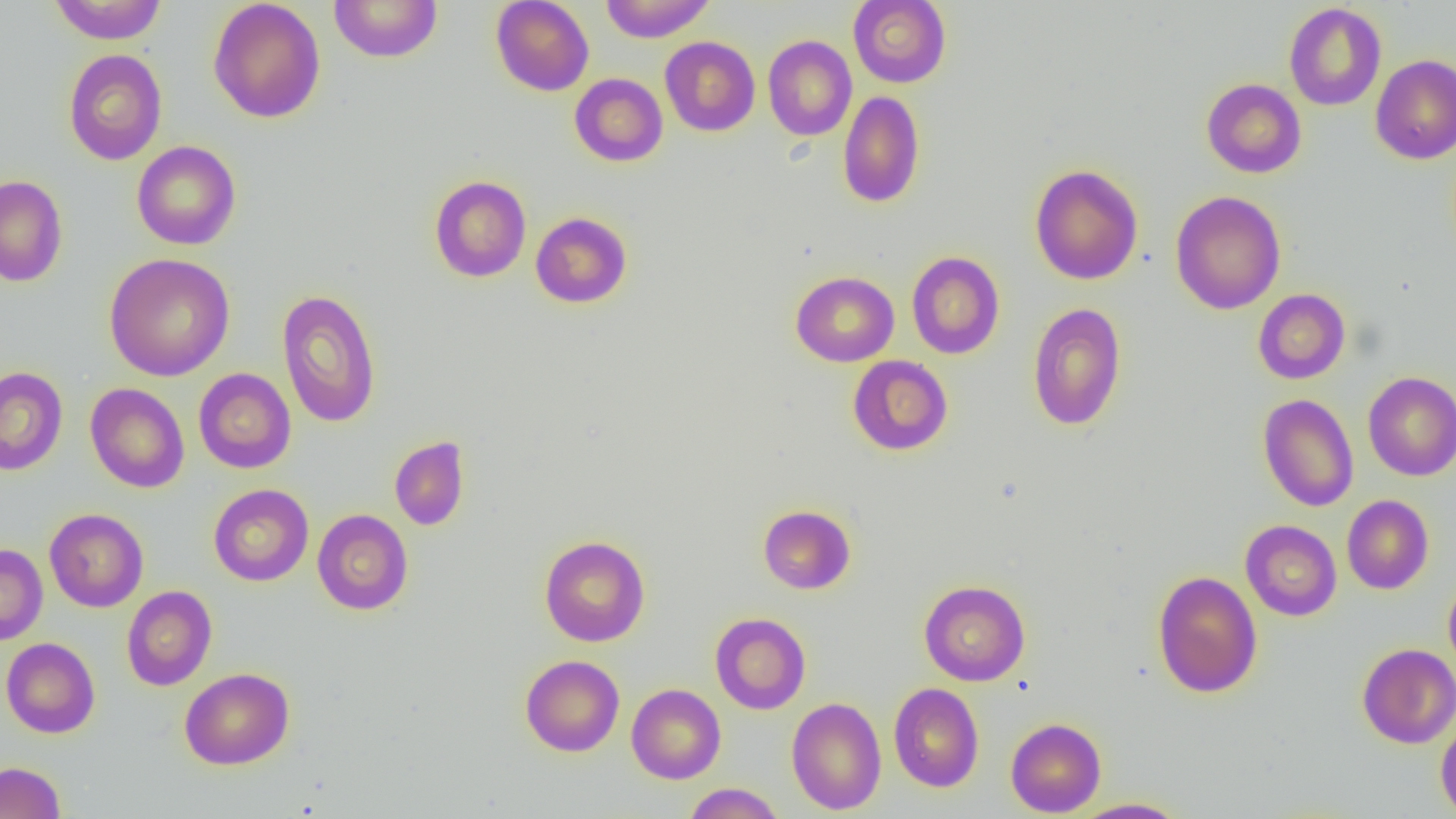

slide-level diagnosis = no evidence of blood parasites
uninfected red blood cell locations = approximate bounding boxes as (x1,y1)-(x2,y2) corner pairs in pixels: (48,0)-(168,44), (208,0)-(326,123), (490,0)-(594,96), (600,0)-(715,42), (848,0)-(951,88), (329,1)-(443,63), (1284,3)-(1386,110), (762,35)-(857,141), (660,36)-(760,136), (63,49)-(167,165), (1370,54)-(1456,165), (569,73)-(668,167), (1201,78)-(1306,178), (838,90)-(925,208), (132,141)-(241,250), (1029,164)-(1144,285), (0,175)-(68,287), (429,175)-(531,282), (1170,190)-(1286,315), (530,212)-(632,308), (906,251)-(1005,359), (104,253)-(236,382), (790,271)-(899,367), (276,288)-(382,428), (1253,289)-(1350,384), (1027,302)-(1127,431), (847,355)-(953,456), (0,366)-(68,475), (193,368)-(296,473), (1363,372)-(1456,481), (85,383)-(190,493), (1258,393)-(1359,512), (389,435)-(470,531), (208,484)-(313,586), (1341,495)-(1433,594), (757,504)-(856,594), (44,508)-(148,612), (312,509)-(413,615), (1241,520)-(1341,621), (539,535)-(650,646), (0,543)-(48,645), (1152,570)-(1263,698), (1443,575)-(1456,677), (918,580)-(1030,686), (121,585)-(217,691), (710,612)-(811,715), (1,637)-(100,738), (1357,643)-(1456,748), (520,654)-(624,757), (179,667)-(295,770), (888,683)-(984,792), (626,684)-(726,784), (787,697)-(886,815), (1435,714)-(1456,819), (1005,717)-(1106,817), (0,761)-(66,819), (683,783)-(785,818), (1070,797)-(1191,818)
modality = light microscopy
preparation = thin blood film
image size = 1456×819 pixels
field of view = single
magnification = 1000x